Classify this cell by malaria status.
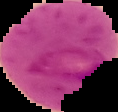
It is parasitized.

Image is 118×112 pixels. From a thin blood smear. Segmented cell region on a black background.